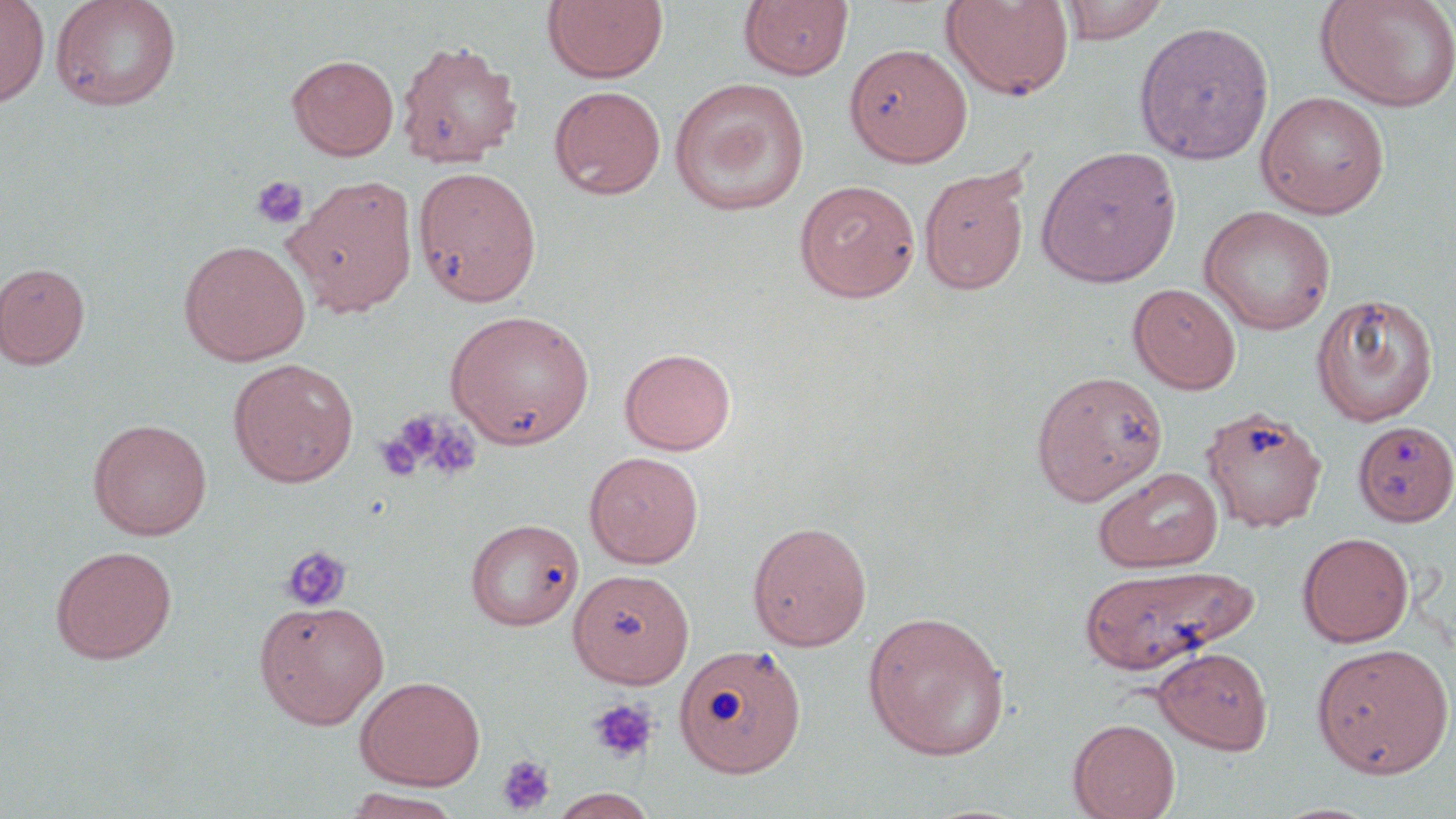

Approximate bounding boxes as named x1/y1/x2/y2 corners in pixels. Uninfected red blood cell locations: (x1=0, y1=0, x2=50, y2=108), (x1=50, y1=0, x2=183, y2=112), (x1=543, y1=0, x2=668, y2=84), (x1=940, y1=0, x2=1075, y2=101), (x1=1059, y1=0, x2=1170, y2=44), (x1=1315, y1=0, x2=1456, y2=113), (x1=739, y1=1, x2=853, y2=81), (x1=1134, y1=21, x2=1274, y2=164), (x1=396, y1=41, x2=521, y2=168), (x1=844, y1=42, x2=972, y2=167), (x1=286, y1=54, x2=399, y2=160), (x1=668, y1=77, x2=810, y2=217), (x1=548, y1=85, x2=666, y2=200), (x1=1255, y1=90, x2=1391, y2=219), (x1=1035, y1=146, x2=1182, y2=288), (x1=413, y1=165, x2=542, y2=307), (x1=918, y1=166, x2=1031, y2=294), (x1=286, y1=175, x2=419, y2=316), (x1=793, y1=179, x2=921, y2=302), (x1=1199, y1=205, x2=1336, y2=335), (x1=178, y1=240, x2=311, y2=365), (x1=0, y1=262, x2=90, y2=369), (x1=1128, y1=283, x2=1242, y2=393), (x1=1310, y1=293, x2=1439, y2=427), (x1=445, y1=309, x2=596, y2=450), (x1=619, y1=347, x2=737, y2=455), (x1=228, y1=358, x2=359, y2=488), (x1=1031, y1=370, x2=1168, y2=505), (x1=1201, y1=406, x2=1328, y2=532), (x1=88, y1=418, x2=213, y2=541), (x1=1353, y1=420, x2=1455, y2=526), (x1=584, y1=450, x2=704, y2=568), (x1=1093, y1=466, x2=1224, y2=573), (x1=465, y1=518, x2=584, y2=630), (x1=747, y1=520, x2=872, y2=651), (x1=1297, y1=532, x2=1414, y2=647), (x1=50, y1=544, x2=177, y2=664), (x1=1078, y1=564, x2=1257, y2=675), (x1=570, y1=567, x2=692, y2=687), (x1=253, y1=598, x2=390, y2=729), (x1=861, y1=610, x2=1011, y2=761), (x1=1311, y1=642, x2=1455, y2=779), (x1=675, y1=643, x2=807, y2=777), (x1=1153, y1=646, x2=1273, y2=754), (x1=354, y1=675, x2=485, y2=790), (x1=1068, y1=718, x2=1180, y2=819), (x1=340, y1=788, x2=465, y2=819), (x1=548, y1=788, x2=659, y2=819). Platelet locations: (x1=251, y1=175, x2=310, y2=230), (x1=377, y1=412, x2=453, y2=480), (x1=281, y1=544, x2=352, y2=612), (x1=587, y1=697, x2=660, y2=764), (x1=496, y1=754, x2=557, y2=816). Slide-level diagnosis: no evidence of blood parasites. Optical microscopy. Image is 1456×819 pixels. Captured at 1000x magnification. Thin blood film. Single field of view. May-Grünwald-Giemsa stain.